State which parasite is depicted.
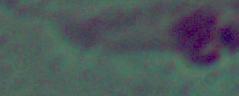

Leishmania.

magnification = 1000x
modality = micrograph